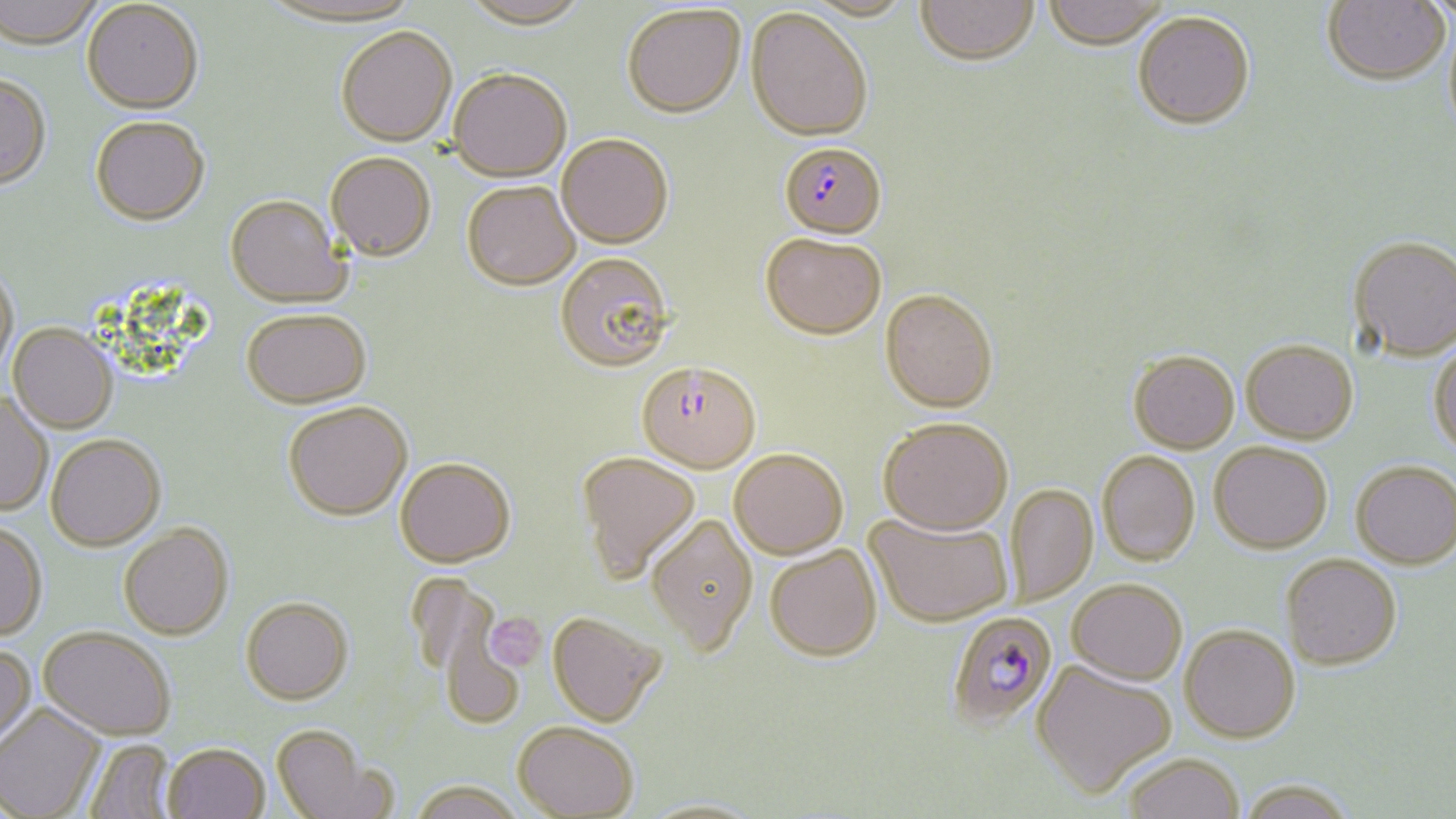 Approximate bounding boxes as (x1,y1)-(x2,y2) corner pairs in pixels. Uninfected red blood cell locations: (0,0)-(104,52), (460,0)-(592,31), (804,0)-(916,22), (916,0)-(1039,66), (1042,0)-(1168,50), (1322,0)-(1450,86), (258,1)-(423,31), (1421,1)-(1456,28), (82,2)-(204,117), (622,4)-(746,119), (746,8)-(873,141), (1133,10)-(1255,128), (335,27)-(457,148), (448,68)-(572,182), (0,77)-(52,192), (90,120)-(210,229), (556,135)-(673,249), (326,154)-(436,264), (462,183)-(580,291), (225,197)-(351,311), (760,232)-(887,338), (1349,235)-(1456,361), (555,253)-(675,373), (0,268)-(19,381), (880,288)-(998,413), (241,312)-(372,411), (8,326)-(117,435), (1241,339)-(1358,443), (1428,340)-(1456,457), (1128,350)-(1239,452), (0,393)-(53,518), (283,402)-(413,521), (878,417)-(1013,534), (46,436)-(166,553), (1209,441)-(1332,553), (729,448)-(848,558), (1097,451)-(1200,565), (576,452)-(700,583), (395,459)-(516,568), (1351,460)-(1455,569), (1006,485)-(1098,605), (864,511)-(1014,626), (645,514)-(757,655), (0,523)-(47,643), (119,525)-(234,643), (765,545)-(882,661), (1280,554)-(1402,669), (1067,579)-(1188,685), (240,597)-(354,706), (547,611)-(666,726), (439,612)-(525,728), (1180,624)-(1300,742), (39,628)-(175,744), (0,644)-(37,756), (1031,659)-(1176,799), (0,705)-(105,819), (512,721)-(639,818), (270,724)-(388,819), (83,739)-(177,819), (163,745)-(269,819), (1122,753)-(1244,819), (1236,779)-(1359,819), (408,780)-(527,819), (638,797)-(766,818). Plasmodium falciparum-infected red blood cell locations: (779,141)-(886,239), (636,361)-(761,473), (946,611)-(1058,731). Platelet locations: (484,612)-(547,672). Slide-level diagnosis: Plasmodium falciparum. May-Grünwald-Giemsa stain. Optical microscopy. One field of a larger specimen. Thin blood smear. 1000x magnification. Image is 1456×819 pixels.